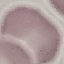
Summary:
  - Malaria status: uninfected
  - Image type: automatically extracted cell patch, resized to 64 × 64 pixels
  - Stain: Giemsa
  - Preparation: thin smear
  - Capture: smartphone camera at the microscope eyepiece